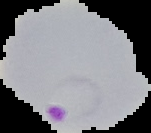
image size = 151×133 pixels
malaria status = parasitized
image type = segmented cell region on a black background
preparation = thin blood smear